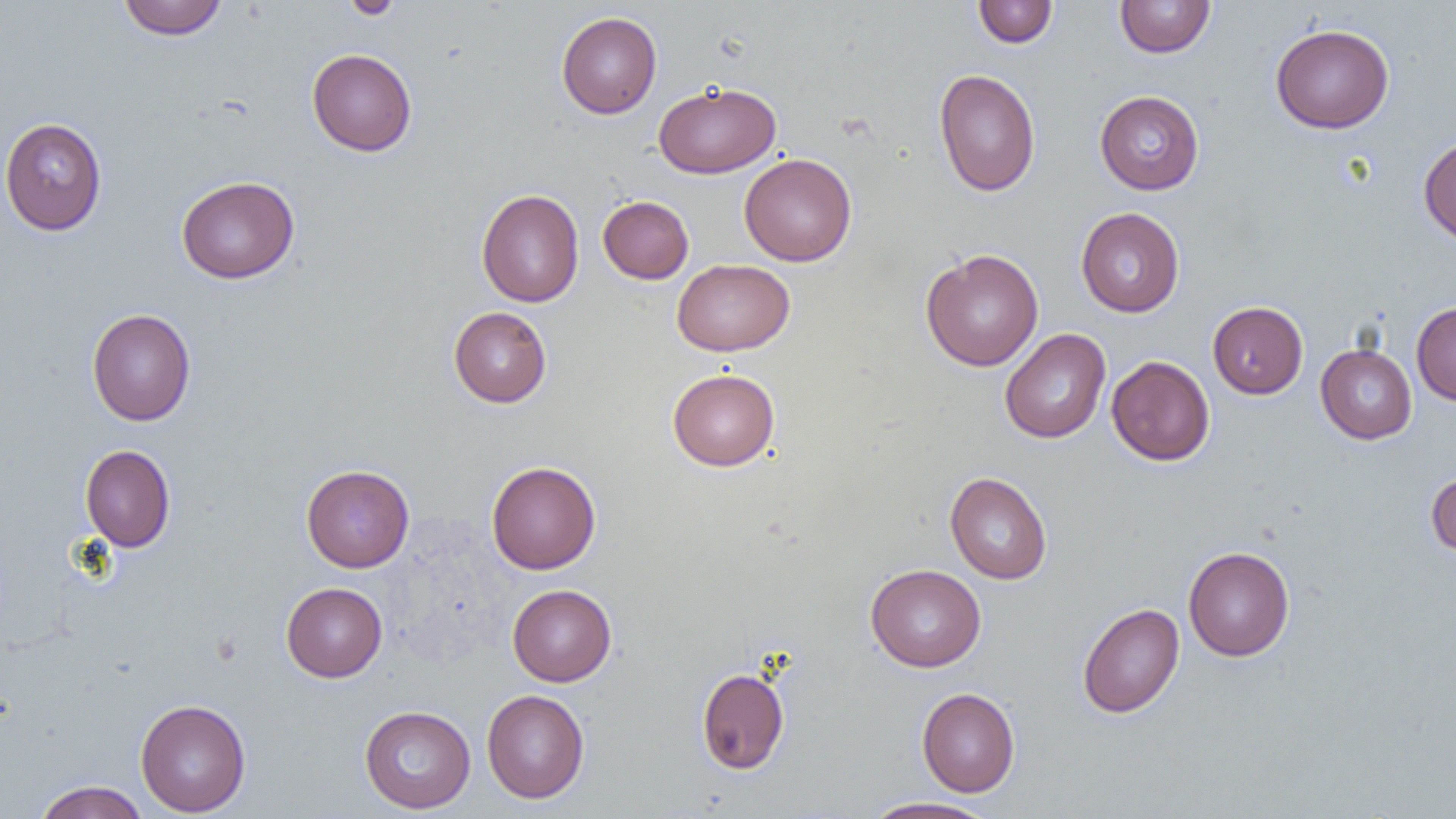
Summary:
  - Coordinate format: approximate bounding boxes as named x1/y1/x2/y2 corners in pixels
  - Uninfected red blood cell locations: (x1=117, y1=0, x2=228, y2=40), (x1=340, y1=0, x2=404, y2=19), (x1=1114, y1=0, x2=1216, y2=58), (x1=973, y1=1, x2=1058, y2=48), (x1=556, y1=11, x2=662, y2=119), (x1=1270, y1=23, x2=1395, y2=133), (x1=307, y1=48, x2=417, y2=156), (x1=934, y1=69, x2=1041, y2=196), (x1=653, y1=81, x2=781, y2=178), (x1=1094, y1=90, x2=1205, y2=195), (x1=0, y1=117, x2=107, y2=235), (x1=1418, y1=135, x2=1456, y2=246), (x1=739, y1=153, x2=856, y2=266), (x1=176, y1=176, x2=299, y2=284), (x1=476, y1=188, x2=584, y2=307), (x1=597, y1=195, x2=694, y2=284), (x1=1076, y1=207, x2=1185, y2=317), (x1=921, y1=248, x2=1044, y2=371), (x1=671, y1=258, x2=795, y2=356), (x1=1207, y1=301, x2=1308, y2=399), (x1=1411, y1=301, x2=1456, y2=405), (x1=449, y1=307, x2=552, y2=407), (x1=86, y1=308, x2=196, y2=425), (x1=999, y1=328, x2=1111, y2=443), (x1=1315, y1=343, x2=1417, y2=444), (x1=1106, y1=356, x2=1215, y2=466), (x1=667, y1=368, x2=780, y2=471), (x1=80, y1=445, x2=175, y2=551), (x1=486, y1=461, x2=601, y2=574), (x1=301, y1=464, x2=414, y2=572), (x1=1425, y1=470, x2=1456, y2=558), (x1=945, y1=472, x2=1052, y2=584), (x1=1183, y1=546, x2=1295, y2=661), (x1=865, y1=564, x2=986, y2=671), (x1=281, y1=582, x2=387, y2=682), (x1=507, y1=584, x2=616, y2=686), (x1=1077, y1=603, x2=1184, y2=718), (x1=696, y1=667, x2=789, y2=774), (x1=917, y1=687, x2=1020, y2=797), (x1=482, y1=690, x2=589, y2=803), (x1=135, y1=698, x2=251, y2=816), (x1=359, y1=705, x2=476, y2=813), (x1=33, y1=781, x2=149, y2=819), (x1=861, y1=796, x2=999, y2=818)
  - Slide-level diagnosis: no evidence of blood parasites
  - Magnification: 1000x
  - Image size: 1456×819 pixels
  - Preparation: thin blood film
  - Modality: light microscopy
  - Field of view: single